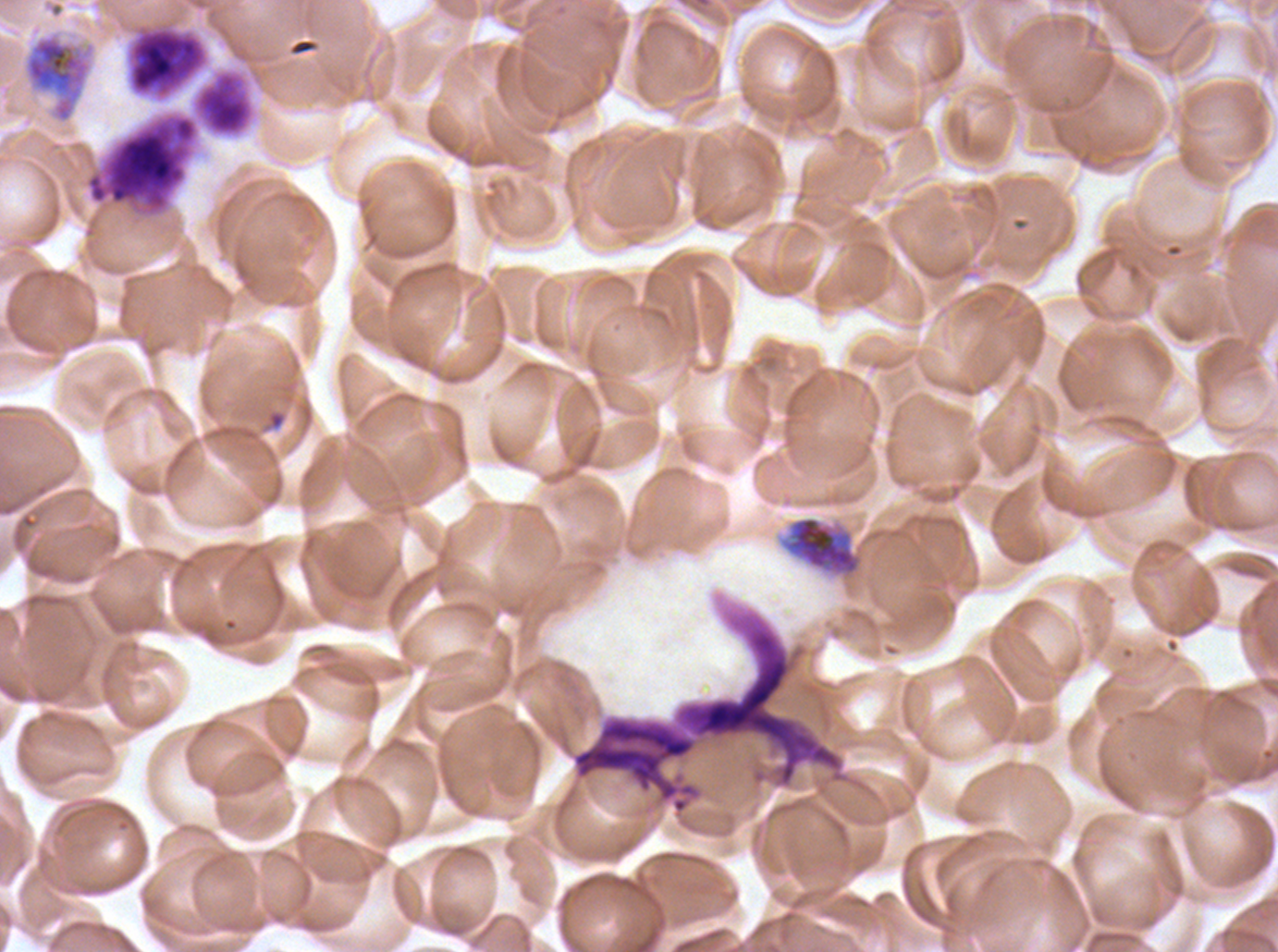
Approximate bounding rectangles given as corner coordinates in pixels from the top-left. Leukocyte locations: (x1=129, y1=28, x2=206, y2=97), (x1=83, y1=67, x2=256, y2=220). Late schizont locations: (x1=778, y1=511, x2=964, y2=581). Debris locations: (x1=571, y1=700, x2=843, y2=814). Segmenter locations: (x1=24, y1=34, x2=91, y2=123). Ex-vivo P. falciparum culture from a patient in The Gambia, grown for 24 to 48 hours. Thin blood smear. Giemsa stain. A sub-image separated from a larger composite. Life-cycle stages observed: late schizont, segmenter. Image is 1278×952 pixels.